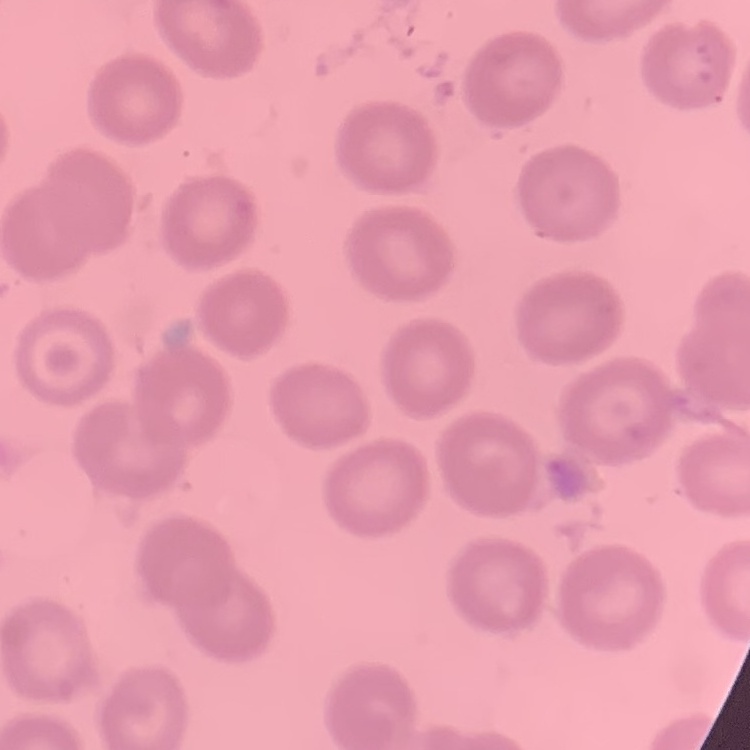 The red blood cells exhibit no rouleaux formation. Square crop of a larger photomicrograph. Field's or Giemsa stain. Thin blood smear.